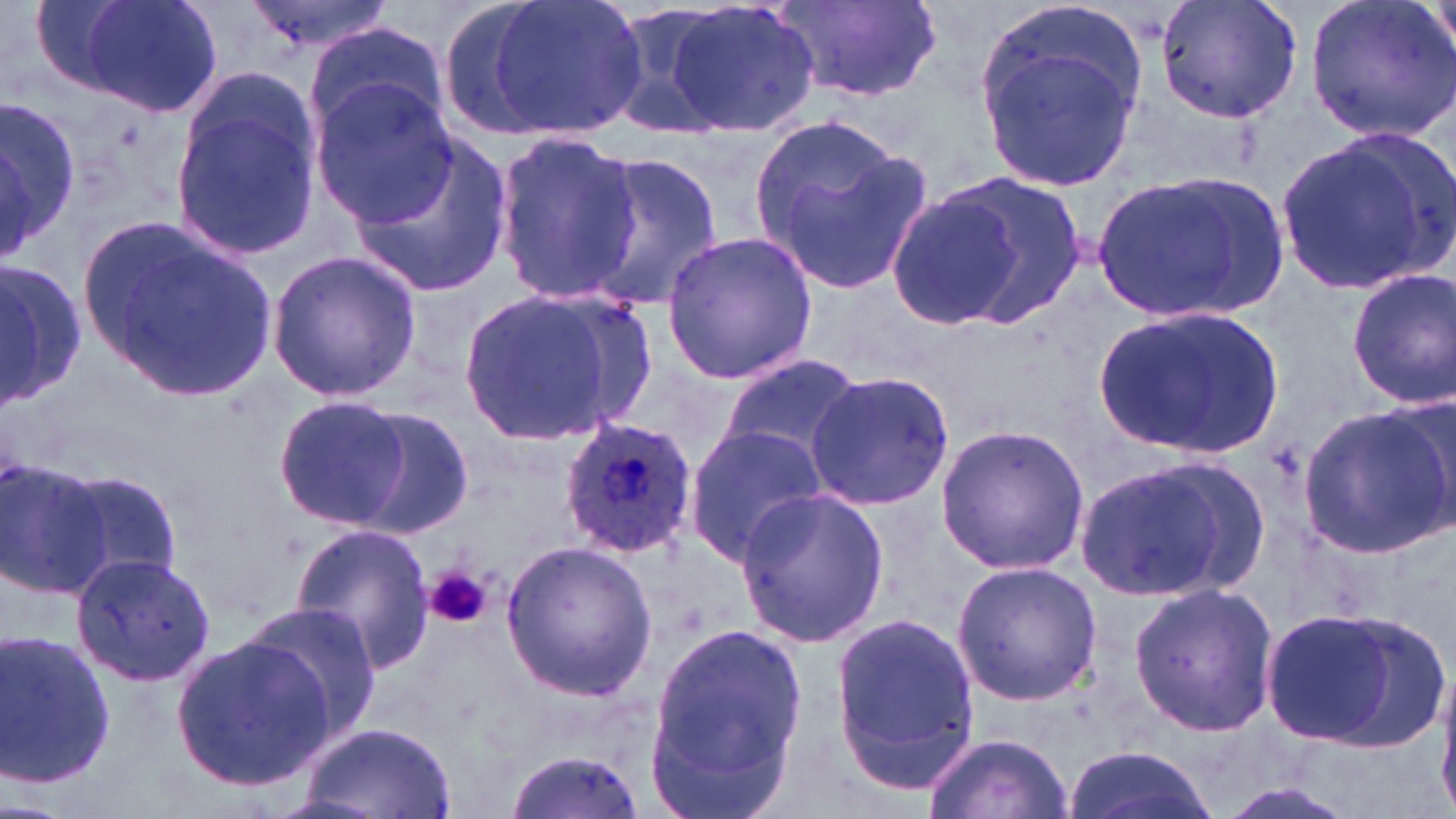
Approximate bounding boxes as [x1, y1, x2, y2] in pixels. Platelet locations: [425, 567, 491, 629]. Plasmodium ovale-infected red blood cell locations: [559, 416, 698, 559]. Uninfected red blood cell locations: [62, 0, 225, 116], [234, 0, 397, 58], [432, 0, 574, 142], [479, 0, 642, 139], [661, 0, 822, 138], [773, 0, 945, 102], [1156, 0, 1301, 126], [1305, 0, 1456, 145], [601, 2, 756, 140], [976, 10, 1145, 189], [305, 25, 447, 135], [308, 78, 456, 226], [0, 97, 77, 259], [170, 102, 323, 259], [746, 109, 931, 298], [350, 130, 515, 300], [1278, 132, 1453, 294], [492, 134, 641, 305], [577, 154, 727, 317], [1087, 170, 1292, 325], [931, 174, 1089, 324], [889, 191, 1022, 327], [85, 220, 276, 405], [662, 231, 820, 383], [266, 250, 421, 403], [0, 263, 90, 407], [1347, 269, 1455, 408], [455, 287, 650, 446], [1095, 308, 1280, 458], [716, 357, 862, 472], [804, 372, 956, 510], [271, 394, 415, 530], [1299, 402, 1452, 560], [348, 407, 476, 538], [934, 423, 1089, 575], [683, 424, 828, 568], [1073, 454, 1257, 604], [0, 456, 113, 599], [55, 468, 183, 589], [733, 485, 888, 648], [288, 523, 435, 672], [501, 540, 658, 699], [72, 551, 216, 688], [952, 561, 1102, 705], [1129, 582, 1281, 736], [237, 603, 382, 744], [1254, 603, 1446, 751], [829, 610, 984, 798], [645, 620, 812, 818], [0, 629, 119, 795], [170, 633, 333, 791], [293, 721, 458, 819], [922, 730, 1071, 818], [1067, 744, 1216, 819], [501, 749, 648, 819]. Slide-level diagnosis: Plasmodium ovale. Light microscopy. Image is 1456×819 pixels. Thin blood film. May-Grünwald-Giemsa stain. 1000x magnification. One field of a larger specimen.